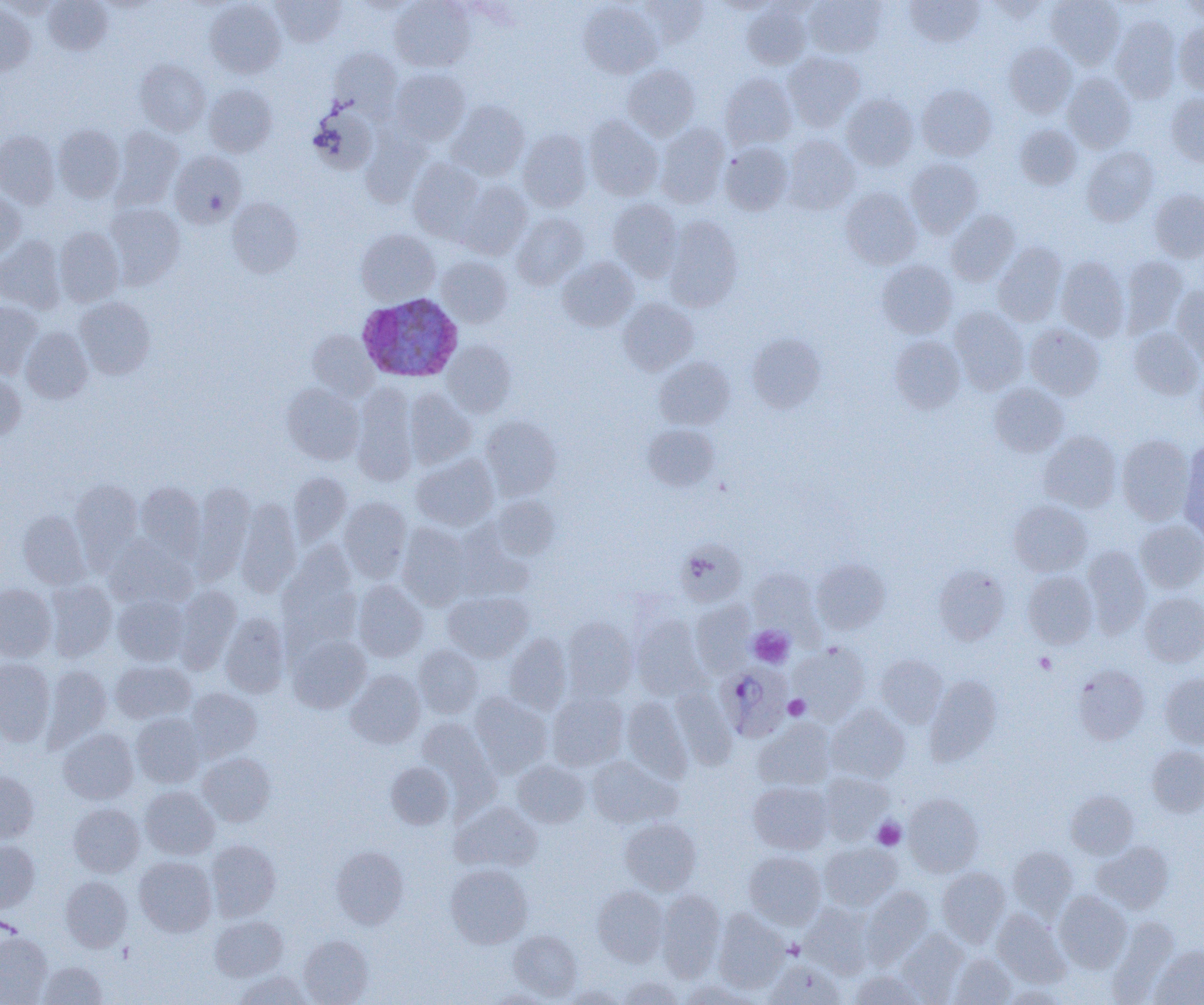

slide_level_diagnosis: Plasmodium ovale
platelet_locations: 'approximate bounding boxes as named x1/y1/x2/y2 corners in pixels: (x1=749, y1=626, x2=794, y2=667), (x1=1034, y1=653, x2=1056, y2=674), (x1=784, y1=695, x2=810, y2=720), (x1=873, y1=818, x2=905, y2=850)'
image_size: 1204×1005 pixels
plasmodium_ovale_infected_red_blood_cell_locations: 'approximate bounding boxes as named x1/y1/x2/y2 corners in pixels: (x1=359, y1=296, x2=466, y2=384), (x1=716, y1=663, x2=793, y2=742)'
field_of_view: single
magnification: 1000x
preparation: thin blood film
uninfected_red_blood_cell_locations: 'approximate bounding boxes as named x1/y1/x2/y2 corners in pixels: (x1=0, y1=0, x2=60, y2=18), (x1=272, y1=0, x2=346, y2=46), (x1=390, y1=0, x2=475, y2=71), (x1=638, y1=0, x2=710, y2=48), (x1=713, y1=0, x2=780, y2=15), (x1=804, y1=0, x2=887, y2=57), (x1=904, y1=0, x2=985, y2=48), (x1=1046, y1=0, x2=1125, y2=69), (x1=1178, y1=0, x2=1204, y2=23), (x1=44, y1=1, x2=112, y2=54), (x1=204, y1=1, x2=286, y2=78), (x1=351, y1=1, x2=420, y2=16), (x1=578, y1=1, x2=661, y2=78), (x1=0, y1=4, x2=35, y2=75), (x1=742, y1=4, x2=811, y2=69), (x1=1110, y1=16, x2=1181, y2=104), (x1=1174, y1=22, x2=1204, y2=95), (x1=1003, y1=42, x2=1077, y2=117), (x1=329, y1=48, x2=402, y2=117), (x1=783, y1=51, x2=865, y2=131), (x1=135, y1=59, x2=210, y2=135), (x1=623, y1=65, x2=700, y2=140), (x1=390, y1=68, x2=470, y2=145), (x1=720, y1=72, x2=797, y2=150), (x1=1062, y1=73, x2=1136, y2=153), (x1=203, y1=84, x2=277, y2=157), (x1=916, y1=84, x2=997, y2=161), (x1=1166, y1=92, x2=1204, y2=166), (x1=841, y1=93, x2=918, y2=170), (x1=448, y1=100, x2=529, y2=181), (x1=308, y1=105, x2=378, y2=175), (x1=584, y1=116, x2=663, y2=200), (x1=655, y1=123, x2=729, y2=208), (x1=54, y1=124, x2=125, y2=202), (x1=1014, y1=124, x2=1081, y2=189), (x1=361, y1=125, x2=431, y2=207), (x1=113, y1=127, x2=184, y2=206), (x1=0, y1=130, x2=59, y2=209), (x1=517, y1=130, x2=592, y2=211), (x1=782, y1=135, x2=860, y2=214), (x1=719, y1=141, x2=793, y2=215), (x1=1082, y1=147, x2=1158, y2=225), (x1=170, y1=150, x2=246, y2=228), (x1=408, y1=158, x2=485, y2=241), (x1=906, y1=158, x2=983, y2=237), (x1=458, y1=182, x2=532, y2=259), (x1=841, y1=188, x2=922, y2=269), (x1=1148, y1=188, x2=1204, y2=263), (x1=0, y1=190, x2=25, y2=262), (x1=228, y1=197, x2=303, y2=277), (x1=608, y1=198, x2=683, y2=279), (x1=106, y1=203, x2=185, y2=288), (x1=946, y1=210, x2=1020, y2=286), (x1=512, y1=212, x2=588, y2=289), (x1=664, y1=216, x2=743, y2=311), (x1=54, y1=227, x2=124, y2=306), (x1=356, y1=229, x2=439, y2=305), (x1=0, y1=236, x2=65, y2=313), (x1=993, y1=242, x2=1067, y2=326), (x1=437, y1=256, x2=512, y2=327), (x1=1055, y1=256, x2=1130, y2=340), (x1=1120, y1=256, x2=1188, y2=336), (x1=557, y1=257, x2=638, y2=331), (x1=877, y1=260, x2=958, y2=338), (x1=1172, y1=284, x2=1204, y2=363), (x1=75, y1=297, x2=155, y2=379), (x1=618, y1=298, x2=698, y2=375), (x1=0, y1=301, x2=43, y2=378), (x1=949, y1=306, x2=1029, y2=394), (x1=1025, y1=323, x2=1105, y2=400), (x1=21, y1=327, x2=93, y2=403), (x1=1129, y1=328, x2=1203, y2=400), (x1=307, y1=330, x2=379, y2=400), (x1=747, y1=333, x2=825, y2=412), (x1=890, y1=335, x2=965, y2=413), (x1=443, y1=340, x2=516, y2=417), (x1=655, y1=357, x2=735, y2=430), (x1=0, y1=373, x2=26, y2=441), (x1=282, y1=383, x2=364, y2=464), (x1=989, y1=383, x2=1069, y2=457), (x1=352, y1=386, x2=418, y2=485), (x1=405, y1=389, x2=477, y2=468), (x1=480, y1=416, x2=561, y2=499), (x1=643, y1=424, x2=719, y2=491), (x1=1039, y1=431, x2=1121, y2=512), (x1=1116, y1=434, x2=1194, y2=524), (x1=1180, y1=441, x2=1204, y2=539), (x1=412, y1=454, x2=498, y2=531), (x1=288, y1=472, x2=352, y2=546), (x1=70, y1=480, x2=142, y2=563), (x1=135, y1=482, x2=205, y2=558), (x1=190, y1=483, x2=255, y2=580), (x1=490, y1=495, x2=561, y2=560), (x1=339, y1=497, x2=412, y2=581), (x1=236, y1=499, x2=301, y2=596), (x1=1009, y1=500, x2=1091, y2=576), (x1=17, y1=511, x2=89, y2=589), (x1=1135, y1=519, x2=1204, y2=593), (x1=397, y1=523, x2=472, y2=608), (x1=452, y1=526, x2=534, y2=601), (x1=106, y1=537, x2=195, y2=608), (x1=675, y1=539, x2=747, y2=607), (x1=1082, y1=545, x2=1151, y2=636), (x1=278, y1=546, x2=361, y2=644), (x1=811, y1=559, x2=890, y2=634), (x1=933, y1=565, x2=1009, y2=645), (x1=748, y1=569, x2=820, y2=636), (x1=1022, y1=571, x2=1098, y2=648), (x1=45, y1=580, x2=117, y2=661), (x1=353, y1=580, x2=429, y2=662), (x1=0, y1=584, x2=56, y2=661), (x1=172, y1=586, x2=241, y2=672), (x1=443, y1=591, x2=532, y2=662), (x1=1139, y1=592, x2=1204, y2=666), (x1=113, y1=596, x2=190, y2=665), (x1=690, y1=601, x2=755, y2=676), (x1=220, y1=613, x2=289, y2=697), (x1=631, y1=616, x2=707, y2=699), (x1=563, y1=617, x2=638, y2=700), (x1=504, y1=633, x2=572, y2=714), (x1=288, y1=634, x2=371, y2=713), (x1=790, y1=643, x2=870, y2=722), (x1=413, y1=644, x2=483, y2=718), (x1=876, y1=654, x2=948, y2=727), (x1=0, y1=659, x2=54, y2=745), (x1=110, y1=660, x2=195, y2=723), (x1=43, y1=664, x2=111, y2=748), (x1=1073, y1=665, x2=1149, y2=744), (x1=346, y1=669, x2=425, y2=749), (x1=1161, y1=674, x2=1204, y2=748), (x1=924, y1=675, x2=1001, y2=765), (x1=671, y1=687, x2=737, y2=770), (x1=186, y1=688, x2=262, y2=760), (x1=547, y1=691, x2=628, y2=770), (x1=470, y1=693, x2=552, y2=776), (x1=621, y1=696, x2=693, y2=782), (x1=826, y1=705, x2=910, y2=783), (x1=131, y1=714, x2=205, y2=787), (x1=417, y1=718, x2=498, y2=802), (x1=754, y1=719, x2=837, y2=790), (x1=58, y1=728, x2=139, y2=804), (x1=1147, y1=745, x2=1204, y2=816), (x1=198, y1=752, x2=276, y2=826), (x1=587, y1=756, x2=680, y2=828), (x1=513, y1=760, x2=590, y2=827), (x1=386, y1=762, x2=454, y2=828), (x1=0, y1=771, x2=39, y2=843), (x1=819, y1=772, x2=893, y2=843), (x1=748, y1=781, x2=833, y2=854), (x1=140, y1=786, x2=219, y2=859), (x1=1066, y1=790, x2=1138, y2=858), (x1=903, y1=793, x2=983, y2=877), (x1=451, y1=801, x2=542, y2=873), (x1=68, y1=803, x2=144, y2=877), (x1=620, y1=818, x2=701, y2=895), (x1=206, y1=839, x2=280, y2=921), (x1=0, y1=840, x2=40, y2=912), (x1=819, y1=842, x2=901, y2=911), (x1=1092, y1=842, x2=1173, y2=914), (x1=331, y1=846, x2=409, y2=929), (x1=1009, y1=846, x2=1078, y2=917), (x1=744, y1=850, x2=826, y2=929), (x1=134, y1=856, x2=216, y2=936), (x1=446, y1=863, x2=532, y2=948), (x1=937, y1=867, x2=1009, y2=946), (x1=60, y1=875, x2=132, y2=951), (x1=592, y1=886, x2=668, y2=966), (x1=861, y1=887, x2=933, y2=966), (x1=657, y1=890, x2=725, y2=979), (x1=1054, y1=891, x2=1132, y2=972), (x1=801, y1=903, x2=875, y2=977), (x1=713, y1=909, x2=789, y2=992), (x1=992, y1=909, x2=1070, y2=987), (x1=210, y1=916, x2=287, y2=981), (x1=1108, y1=917, x2=1179, y2=1002), (x1=508, y1=929, x2=582, y2=1000), (x1=896, y1=930, x2=968, y2=1002), (x1=0, y1=932, x2=52, y2=1005), (x1=299, y1=935, x2=373, y2=1005), (x1=1150, y1=947, x2=1204, y2=1005), (x1=950, y1=953, x2=1016, y2=1004), (x1=765, y1=959, x2=846, y2=1005), (x1=37, y1=961, x2=107, y2=1004), (x1=850, y1=970, x2=927, y2=1004), (x1=235, y1=971, x2=311, y2=1005), (x1=619, y1=977, x2=684, y2=1004), (x1=682, y1=980, x2=756, y2=1005), (x1=1001, y1=984, x2=1070, y2=1005), (x1=560, y1=985, x2=627, y2=1005), (x1=485, y1=988, x2=557, y2=1005)'
modality: light microscopy